Assess this cell for malaria.
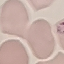
Uninfected.

Photographed with a smartphone camera at the microscope eyepiece. Giemsa stain. Thin smear of blood. Automatically extracted cell patch, resized to 64 × 64 pixels.